Classify this cell by malaria status.
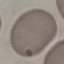
It is uninfected.

stain = Giemsa
preparation = thin blood film
capture = smartphone through the microscope eyepiece
image type = cell patch, automatically extracted from a larger field of view and resized to 64 × 64 pixels